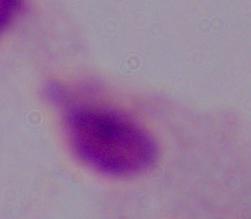

Summary:
  - Modality: micrograph
  - Identification: trichomonad
  - Magnification: 1000x